State which parasite is depicted.
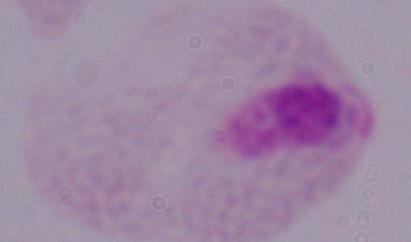

A trichomonad.

Captured at 1000x magnification. Photomicrograph.